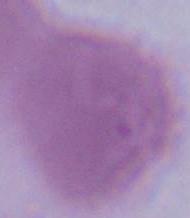
1000x magnification. Photomicrograph. An erythrocyte is shown.